Point out each malaria parasite.
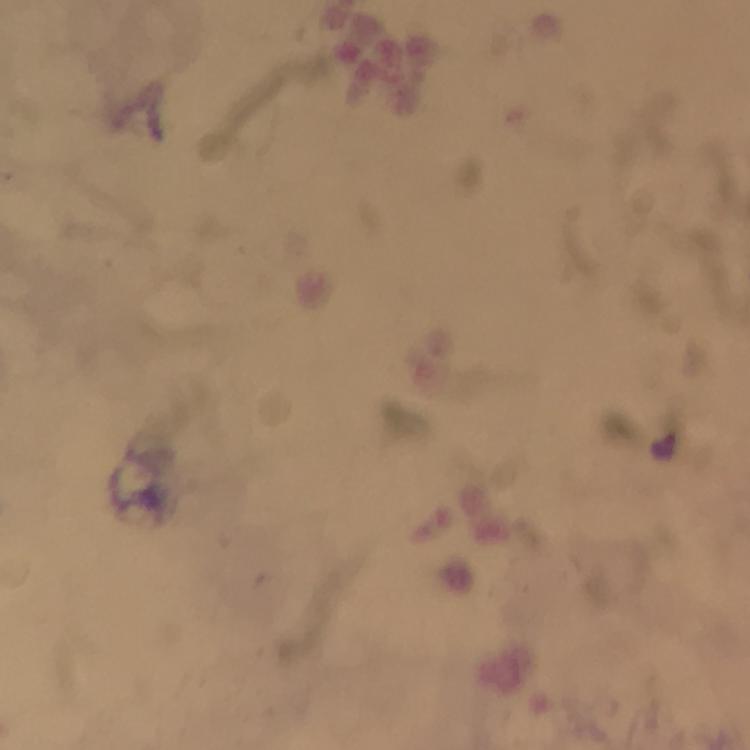

Approximate centers as (x, y) in pixels.
Malaria parasites: (664, 444).

preparation: thick blood smear
magnification: 100x
cropped_from: a single field of view
image_size: 750×750 pixels
context: from a malaria diagnostic workup
capture: smartphone mounted on the microscope
immersion_oil: applied
stain: Giemsa